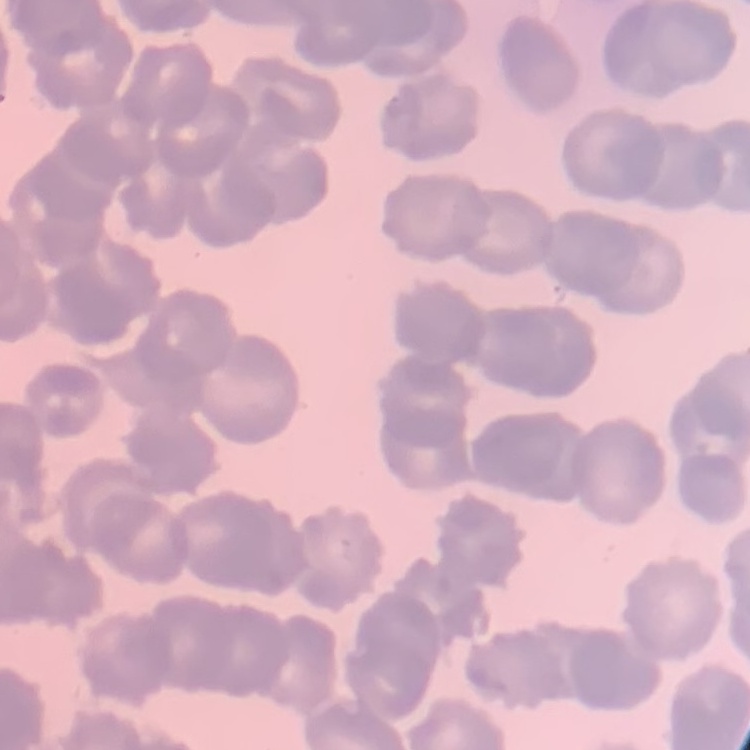
red blood cell morphology = rouleaux formation
stain = Field's or Giemsa
preparation = thin peripheral smear
image type = square crop of a larger photomicrograph